Give the position of every malaria parasite.
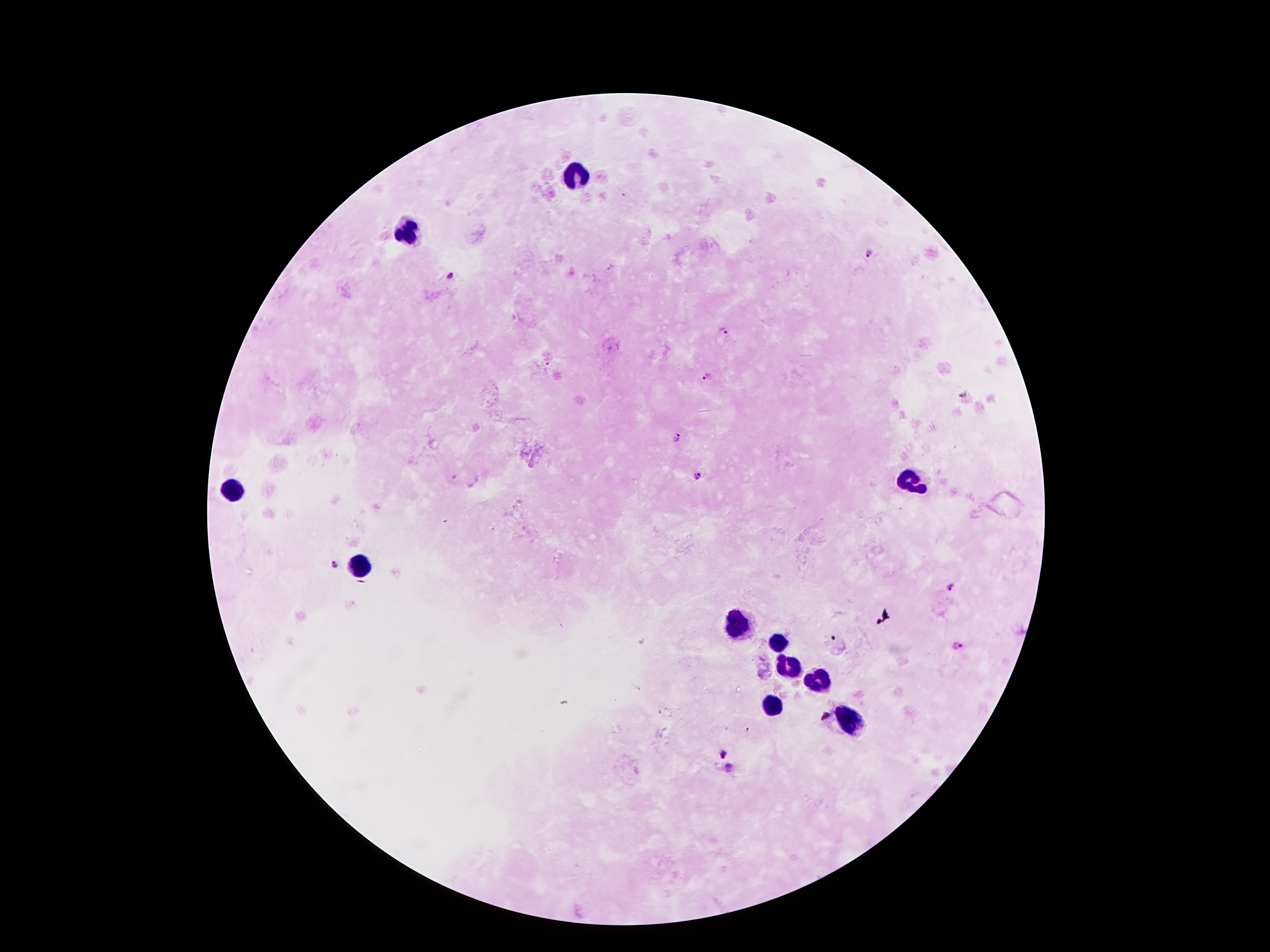
Approximate centers as {x, y} in pixels.
Malaria parasites: {869, 254}, {452, 278}, {724, 332}, {711, 377}, {679, 436}, {696, 476}, {335, 566}, {952, 587}, {960, 647}, {724, 754}, {728, 768}.

Leukocyte locations: {578, 177}, {410, 228}, {910, 477}, {232, 488}, {360, 566}, {735, 620}, {777, 643}, {790, 664}, {821, 679}, {773, 702}, {849, 719}. Image is 1270×952 pixels. 100x magnification. Single field of view. Giemsa stain. Photographed through the microscope eyepiece with a smartphone camera. Patient malaria status: infected with Plasmodium falciparum. Thick peripheral-blood smear.